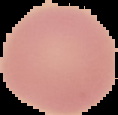
Summary:
  - Image size: 118×115 pixels
  - Malaria status: uninfected
  - Preparation: thin blood film
  - Image type: segmented cell region on a black background